Identify the parasite.
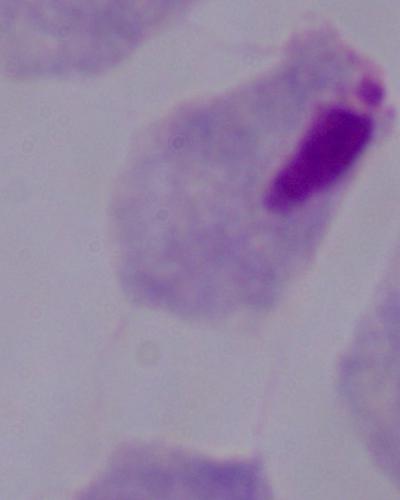

A trichomonad.

magnification = 1000x
modality = photomicrograph